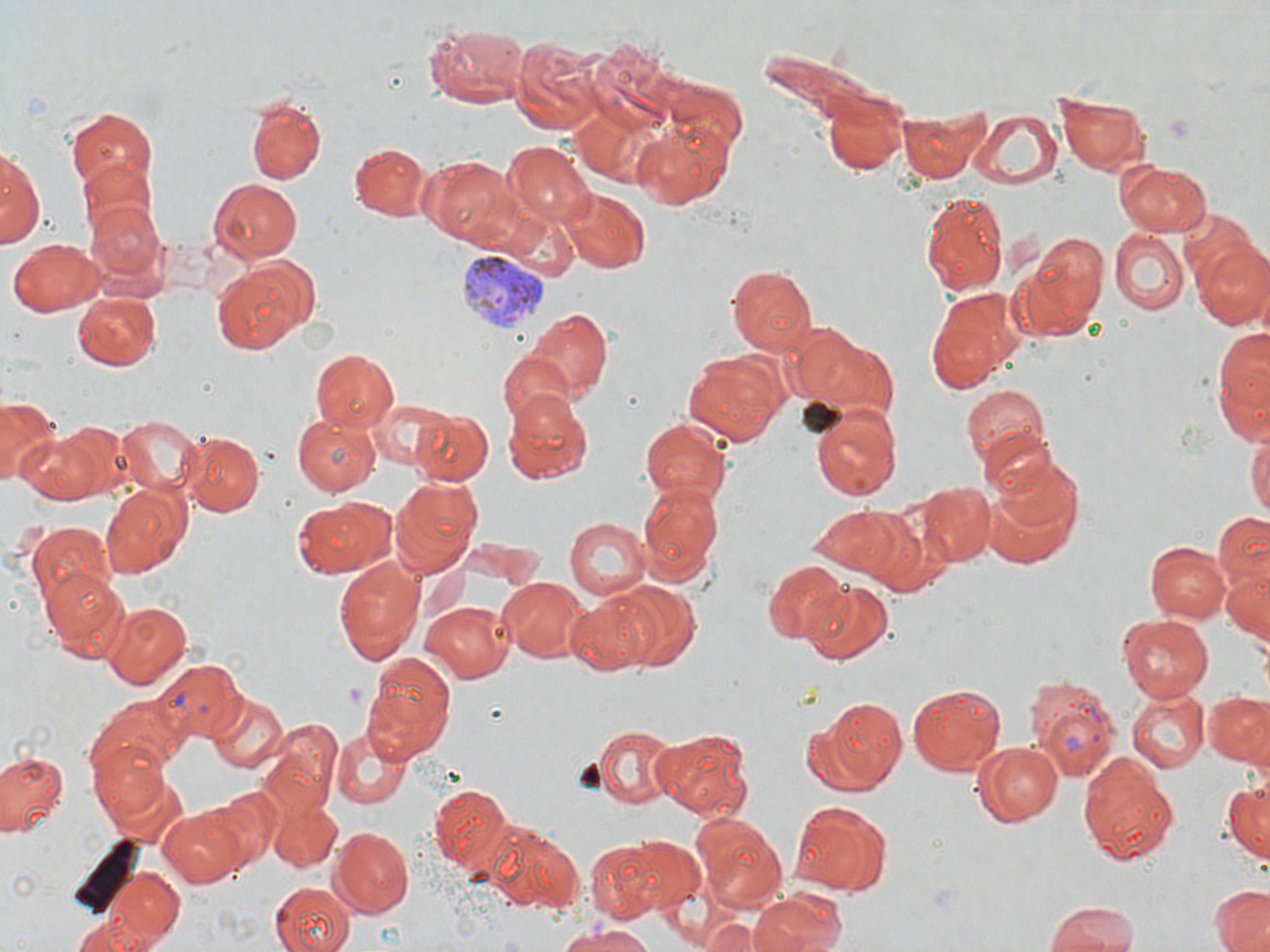
Approximate bounding boxes as named x1/y1/x2/y2 corners in pixels. Plasmodium vivax-infected red blood cell locations: (x1=458, y1=250, x2=548, y2=332), (x1=155, y1=659, x2=245, y2=743), (x1=1024, y1=674, x2=1119, y2=783). Uninfected red blood cell locations: (x1=422, y1=22, x2=527, y2=111), (x1=505, y1=35, x2=607, y2=131), (x1=820, y1=85, x2=914, y2=180), (x1=1054, y1=92, x2=1151, y2=174), (x1=244, y1=93, x2=326, y2=184), (x1=65, y1=107, x2=157, y2=195), (x1=966, y1=108, x2=1064, y2=190), (x1=899, y1=111, x2=984, y2=182), (x1=632, y1=121, x2=732, y2=209), (x1=347, y1=142, x2=433, y2=223), (x1=504, y1=142, x2=596, y2=225), (x1=1, y1=144, x2=42, y2=250), (x1=423, y1=156, x2=520, y2=251), (x1=1115, y1=158, x2=1212, y2=238), (x1=77, y1=160, x2=159, y2=247), (x1=208, y1=176, x2=304, y2=264), (x1=558, y1=188, x2=652, y2=274), (x1=920, y1=190, x2=1007, y2=299), (x1=86, y1=198, x2=164, y2=284), (x1=1111, y1=230, x2=1191, y2=316), (x1=1030, y1=232, x2=1111, y2=322), (x1=10, y1=237, x2=106, y2=314), (x1=1192, y1=237, x2=1270, y2=331), (x1=1010, y1=251, x2=1098, y2=345), (x1=213, y1=257, x2=316, y2=351), (x1=725, y1=264, x2=817, y2=357), (x1=925, y1=287, x2=1023, y2=393), (x1=73, y1=293, x2=160, y2=372), (x1=525, y1=307, x2=614, y2=400), (x1=792, y1=326, x2=900, y2=422), (x1=1213, y1=326, x2=1270, y2=439), (x1=311, y1=349, x2=400, y2=434), (x1=682, y1=350, x2=789, y2=445), (x1=496, y1=351, x2=576, y2=431), (x1=957, y1=383, x2=1053, y2=477), (x1=502, y1=391, x2=593, y2=484), (x1=0, y1=397, x2=58, y2=487), (x1=370, y1=398, x2=459, y2=475), (x1=807, y1=402, x2=902, y2=499), (x1=408, y1=407, x2=494, y2=484), (x1=117, y1=413, x2=203, y2=495), (x1=291, y1=413, x2=381, y2=496), (x1=638, y1=418, x2=733, y2=502), (x1=55, y1=420, x2=138, y2=498), (x1=1247, y1=424, x2=1270, y2=526), (x1=177, y1=430, x2=266, y2=518), (x1=17, y1=431, x2=108, y2=504), (x1=991, y1=450, x2=1086, y2=546), (x1=389, y1=480, x2=482, y2=577), (x1=636, y1=481, x2=723, y2=585), (x1=99, y1=482, x2=190, y2=577), (x1=916, y1=482, x2=995, y2=566), (x1=981, y1=486, x2=1078, y2=566), (x1=290, y1=497, x2=395, y2=579), (x1=826, y1=504, x2=941, y2=589), (x1=1213, y1=512, x2=1270, y2=591), (x1=562, y1=516, x2=650, y2=602), (x1=25, y1=523, x2=118, y2=612), (x1=1146, y1=540, x2=1230, y2=624), (x1=333, y1=552, x2=427, y2=662), (x1=762, y1=560, x2=845, y2=643), (x1=1223, y1=564, x2=1270, y2=642), (x1=43, y1=568, x2=132, y2=658), (x1=498, y1=579, x2=587, y2=663), (x1=613, y1=580, x2=702, y2=670), (x1=800, y1=580, x2=897, y2=667), (x1=565, y1=590, x2=660, y2=677), (x1=104, y1=600, x2=191, y2=689), (x1=422, y1=601, x2=513, y2=682), (x1=1118, y1=613, x2=1215, y2=700), (x1=359, y1=651, x2=456, y2=762), (x1=906, y1=682, x2=1006, y2=776), (x1=1125, y1=686, x2=1211, y2=773), (x1=1202, y1=690, x2=1269, y2=765), (x1=205, y1=693, x2=287, y2=775), (x1=87, y1=695, x2=188, y2=785), (x1=803, y1=695, x2=909, y2=797), (x1=263, y1=719, x2=342, y2=816), (x1=590, y1=722, x2=680, y2=806), (x1=332, y1=725, x2=411, y2=808), (x1=653, y1=726, x2=755, y2=822), (x1=90, y1=737, x2=174, y2=832), (x1=971, y1=740, x2=1063, y2=827), (x1=0, y1=749, x2=68, y2=839), (x1=1078, y1=751, x2=1181, y2=866), (x1=1221, y1=781, x2=1269, y2=862), (x1=428, y1=782, x2=514, y2=875), (x1=206, y1=787, x2=285, y2=870), (x1=264, y1=788, x2=343, y2=871), (x1=787, y1=798, x2=893, y2=895), (x1=159, y1=805, x2=250, y2=888), (x1=693, y1=814, x2=787, y2=910), (x1=482, y1=822, x2=583, y2=914), (x1=331, y1=824, x2=413, y2=915), (x1=588, y1=831, x2=704, y2=924), (x1=91, y1=861, x2=191, y2=946), (x1=267, y1=880, x2=356, y2=952), (x1=1209, y1=884, x2=1270, y2=952), (x1=746, y1=889, x2=851, y2=952), (x1=1042, y1=901, x2=1141, y2=952), (x1=693, y1=913, x2=782, y2=951), (x1=72, y1=914, x2=162, y2=951), (x1=558, y1=924, x2=662, y2=952). Slide-level diagnosis: Plasmodium vivax. 1000x magnification. Optical microscopy. One field of a larger specimen. Thin blood smear. Image is 1270×952 pixels. May-Grünwald-Giemsa stain.